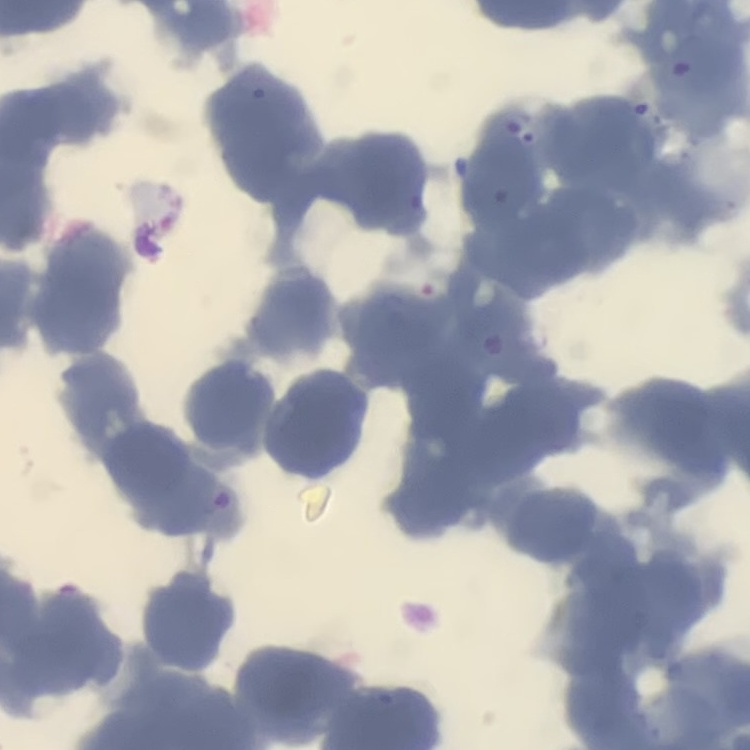
red blood cell morphology = rouleaux formation
preparation = thin peripheral smear
image type = square crop of a larger photomicrograph
stain = Field's or Giemsa